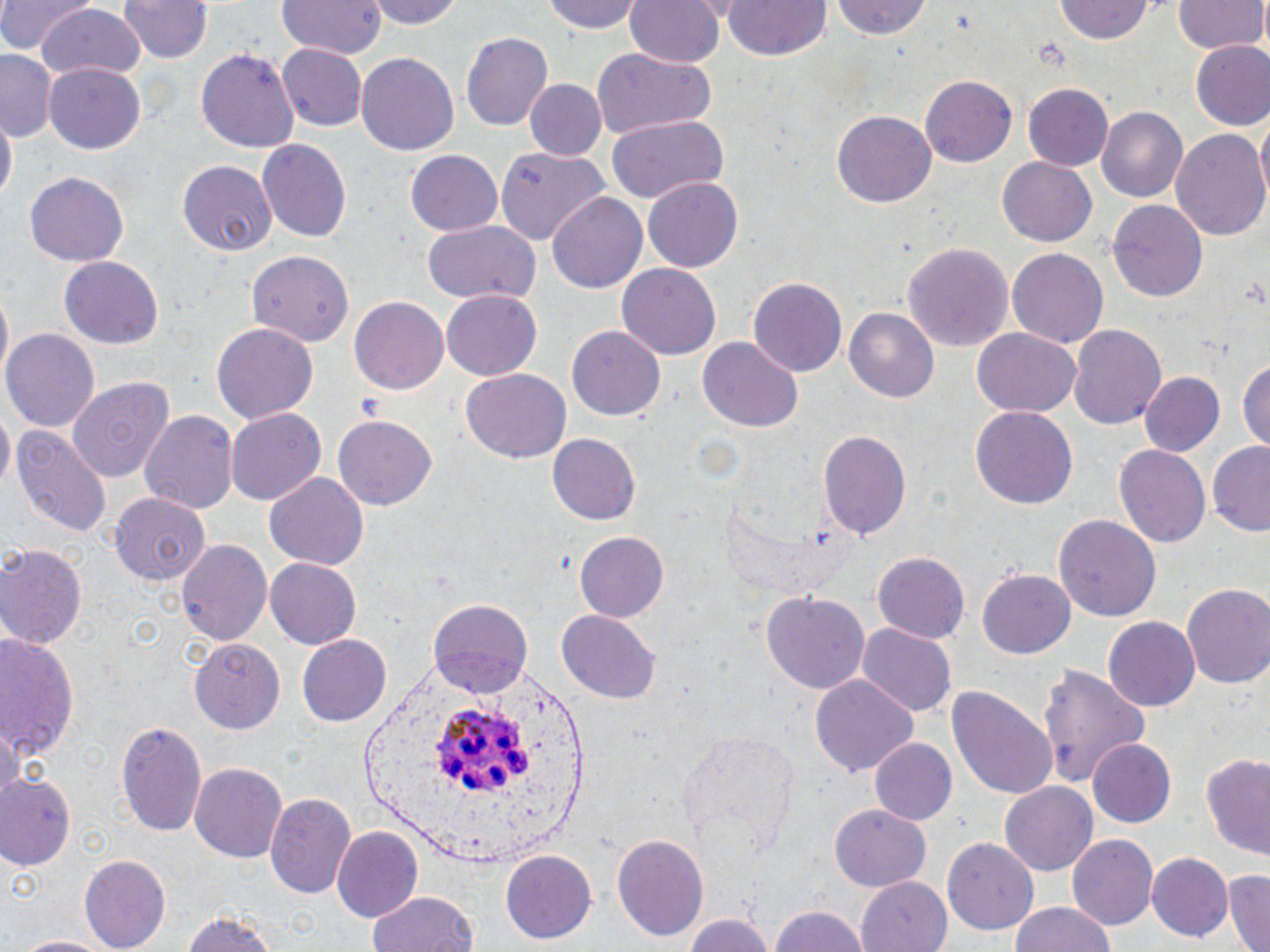
slide-level diagnosis = Plasmodium ovale
preparation = thin blood film
stain = May-Grünwald-Giemsa
field of view = single
modality = optical microscopy
Plasmodium ovale-infected red blood cell locations = approximate bounding boxes as [x1, y1, x2, y2] in pixels: [428, 706, 542, 800]
image size = 1270×952 pixels
uninfected red blood cell locations = approximate bounding boxes as [x1, y1, x2, y2] in pixels: [0, 0, 93, 54], [118, 0, 212, 63], [278, 0, 385, 58], [367, 0, 464, 30], [543, 0, 645, 34], [625, 0, 725, 69], [829, 0, 934, 41], [1175, 0, 1267, 55], [725, 1, 830, 61], [1055, 1, 1154, 44], [35, 6, 146, 84], [461, 33, 553, 130], [1189, 41, 1270, 132], [278, 44, 367, 131], [195, 46, 300, 153], [0, 48, 56, 142], [591, 49, 718, 136], [355, 51, 460, 158], [44, 63, 147, 152], [921, 74, 1019, 168], [524, 78, 606, 161], [1024, 82, 1113, 170], [1098, 106, 1191, 203], [833, 110, 936, 207], [2, 112, 17, 207], [608, 115, 727, 202], [1254, 115, 1270, 211], [1171, 128, 1270, 245], [257, 139, 352, 242], [495, 146, 612, 244], [405, 150, 503, 236], [996, 156, 1097, 247], [176, 160, 276, 256], [24, 173, 131, 267], [643, 175, 743, 270], [545, 190, 649, 295], [1109, 198, 1208, 303], [423, 222, 540, 305], [904, 242, 1012, 354], [1008, 249, 1106, 350], [244, 251, 352, 346], [60, 258, 163, 347], [615, 263, 721, 360], [750, 277, 847, 379], [1, 288, 13, 380], [439, 291, 545, 380], [350, 296, 450, 394], [845, 308, 940, 405], [211, 323, 318, 426], [1069, 324, 1167, 433], [567, 326, 664, 421], [972, 327, 1081, 416], [4, 329, 100, 431], [698, 339, 803, 432], [1237, 356, 1268, 455], [461, 366, 571, 464], [1139, 370, 1226, 457], [66, 378, 174, 484], [0, 405, 14, 492], [970, 405, 1076, 507], [139, 409, 239, 513], [227, 409, 326, 507], [332, 414, 437, 511], [12, 426, 112, 537], [818, 428, 912, 543], [545, 433, 642, 527], [1114, 443, 1211, 549], [1207, 443, 1270, 535], [264, 473, 368, 568], [107, 491, 209, 589], [1054, 515, 1161, 625], [574, 533, 669, 620], [176, 539, 272, 649], [0, 544, 85, 652], [872, 551, 973, 641], [264, 556, 360, 648], [977, 570, 1074, 661], [1181, 583, 1270, 689], [762, 591, 869, 694], [430, 600, 531, 700], [556, 610, 663, 703], [1104, 616, 1198, 712], [856, 622, 956, 717], [0, 631, 83, 763], [295, 634, 391, 728], [188, 639, 284, 735], [1038, 663, 1153, 787], [810, 675, 918, 778], [946, 685, 1058, 799], [115, 721, 208, 836], [0, 723, 26, 812], [677, 729, 798, 847], [869, 736, 958, 825], [1088, 739, 1177, 827], [1202, 751, 1268, 860], [189, 762, 288, 862], [1, 772, 78, 871], [999, 781, 1099, 875], [265, 792, 356, 898], [829, 805, 929, 890], [330, 827, 421, 921], [611, 834, 709, 940], [1067, 834, 1162, 930], [942, 837, 1039, 936], [500, 850, 595, 944], [1148, 852, 1232, 941], [78, 854, 171, 950], [1223, 870, 1270, 952], [858, 876, 953, 952], [367, 889, 480, 952], [1009, 901, 1118, 952], [766, 906, 871, 952], [178, 908, 284, 952], [679, 909, 775, 952], [13, 933, 120, 952]
magnification = 1000x